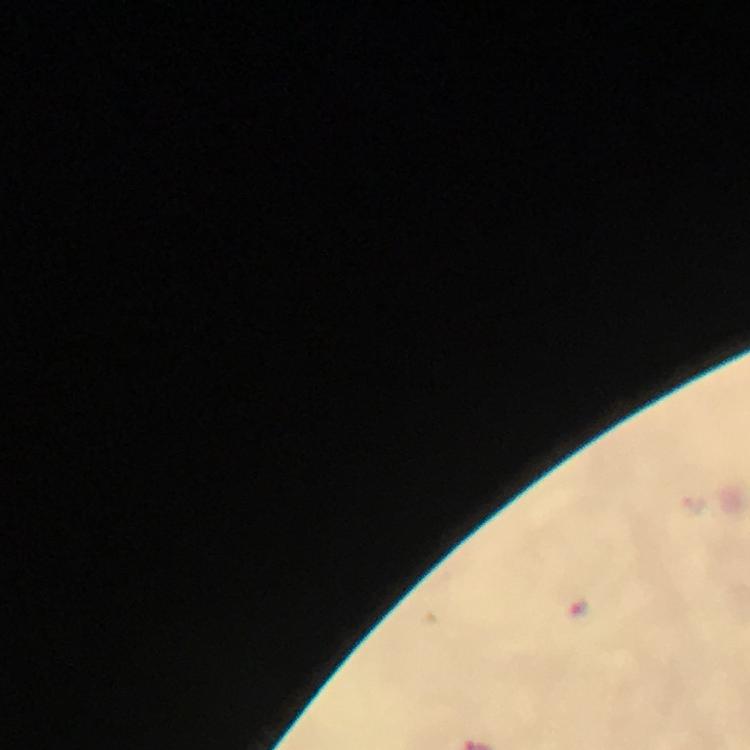
Approximate centers as [x, y] in pixels. Malaria parasite locations: [577, 609]. Giemsa-stained preparation. From a diagnostic examination for malaria. Immersion oil applied. Image is 750×750 pixels. Cropped region of a single field of view. At 100x magnification. Thick smear. Smartphone photograph taken through a microscope.